Locate every blood parasite and identify its species.
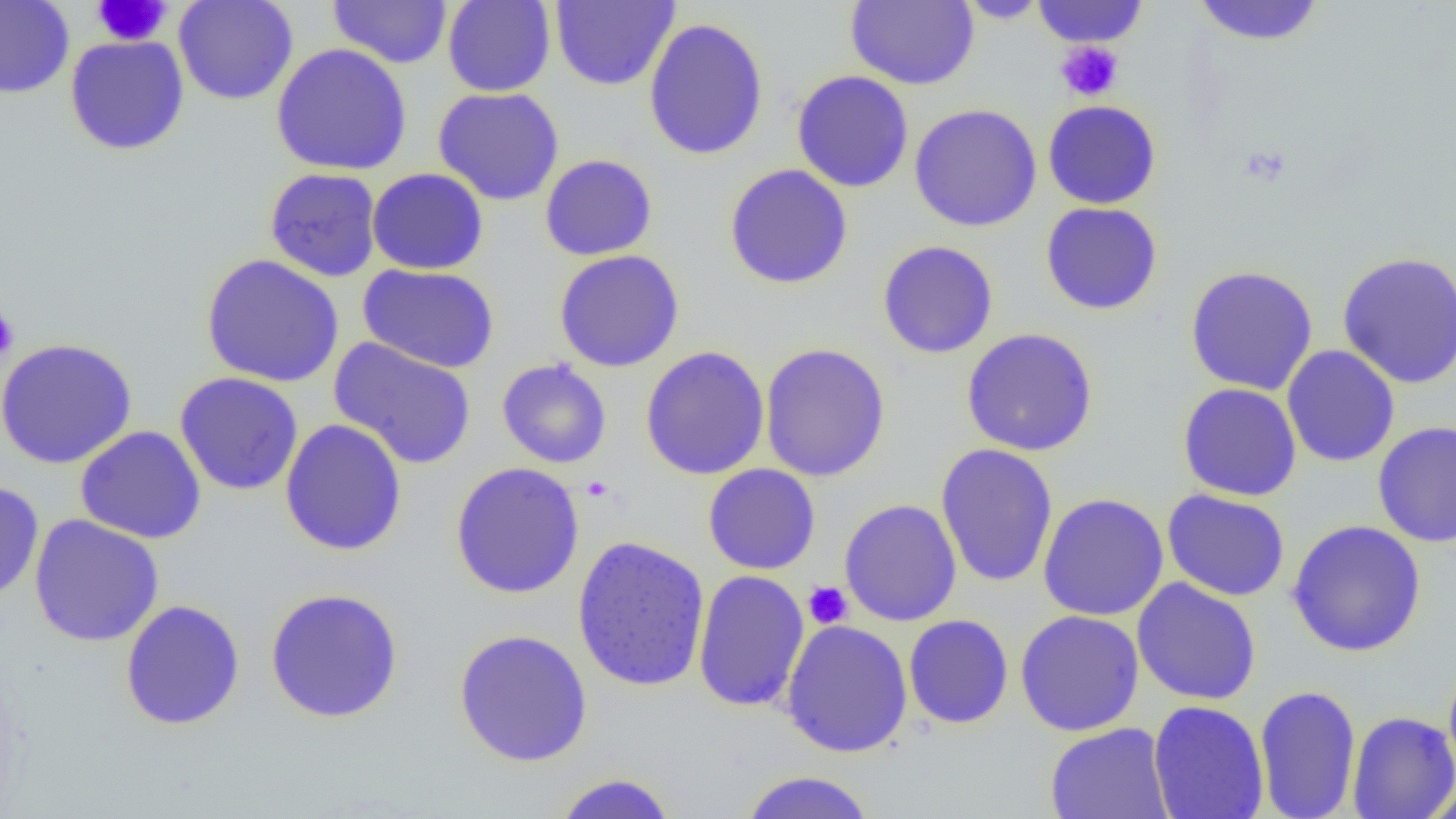
No blood parasites observed.

slide-level diagnosis = negative for blood parasites
modality = light microscopy
uninfected red blood cell locations = approximate bounding boxes as (x1,y1)-(x2,y2) corner pairs in pixels: (173,0)-(299,105), (327,0)-(452,68), (442,0)-(556,97), (1031,0)-(1148,48), (0,1)-(74,99), (550,1)-(680,91), (845,1)-(979,90), (954,1)-(1053,23), (1191,1)-(1326,46), (643,17)-(769,161), (65,35)-(190,156), (271,43)-(412,176), (791,70)-(914,193), (432,87)-(565,206), (1042,100)-(1161,209), (909,103)-(1042,232), (540,154)-(657,260), (724,163)-(854,289), (265,168)-(383,282), (367,168)-(489,275), (1040,201)-(1163,316), (877,240)-(999,359), (554,249)-(685,372), (1336,251)-(1456,390), (201,253)-(344,388), (357,263)-(500,373), (1185,264)-(1319,396), (960,328)-(1098,456), (0,337)-(138,469), (329,337)-(477,470), (759,342)-(891,483), (1282,345)-(1400,467), (640,346)-(770,480), (496,358)-(612,469), (174,372)-(304,496), (1177,382)-(1303,502), (280,418)-(407,556), (1373,421)-(1456,547), (76,426)-(207,544), (935,443)-(1058,587), (449,461)-(585,599), (703,464)-(821,575), (0,480)-(44,604), (1161,489)-(1290,602), (1038,492)-(1169,621), (839,499)-(962,626), (28,514)-(165,647), (1286,519)-(1426,657), (571,535)-(710,693), (692,570)-(810,712), (1132,578)-(1261,705), (264,588)-(404,723), (120,598)-(246,730), (1015,609)-(1145,737), (903,614)-(1014,729), (780,619)-(914,758), (453,629)-(593,767), (1443,658)-(1456,784), (1254,684)-(1361,819), (1148,700)-(1269,819), (1347,711)-(1456,818), (1044,722)-(1175,819), (736,770)-(878,819), (551,772)-(677,819), (1421,780)-(1456,819)
field of view = single
platelet locations = approximate bounding boxes as (x1,y1)-(x2,y2) corner pairs in pixels: (92,0)-(171,46), (1056,40)-(1124,102), (0,307)-(19,363), (803,582)-(853,629)
preparation = thin blood film
magnification = 1000x
image size = 1456×819 pixels